Classify this cell by malaria status.
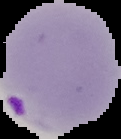
It is parasitized.

image_size: 121×139 pixels
preparation: thin blood smear
image_type: segmented cell region on a black background